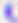
modality = photomicrograph
identification = Toxoplasma gondii
magnification = 400x